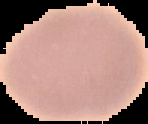

image_size: 148×124 pixels
malaria_status: uninfected
preparation: thin blood film
image_type: segmented cell region on a black background